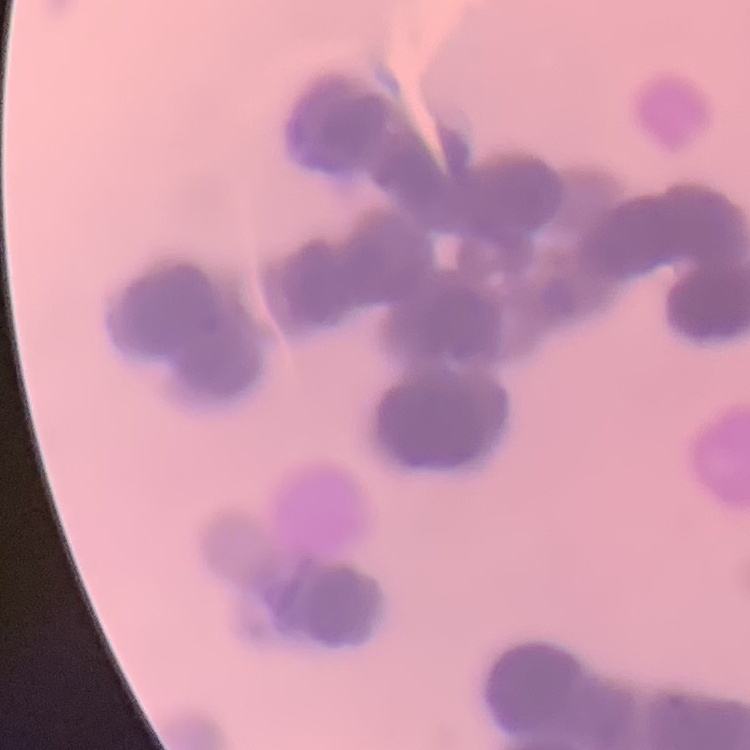 The erythrocytes show rouleaux formation. Thin blood film. Field's or Giemsa stain. One tile cut from a larger photomicrograph.